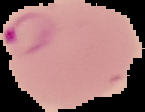

image_type: segmented cell region with the area outside set to black
image_size: 145×112 pixels
malaria_status: parasitized
preparation: thin blood film